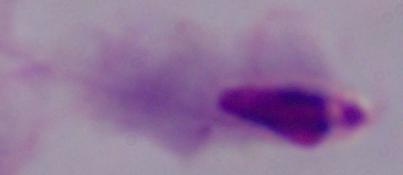

identification: trichomonad
magnification: 1000x
modality: photomicrograph